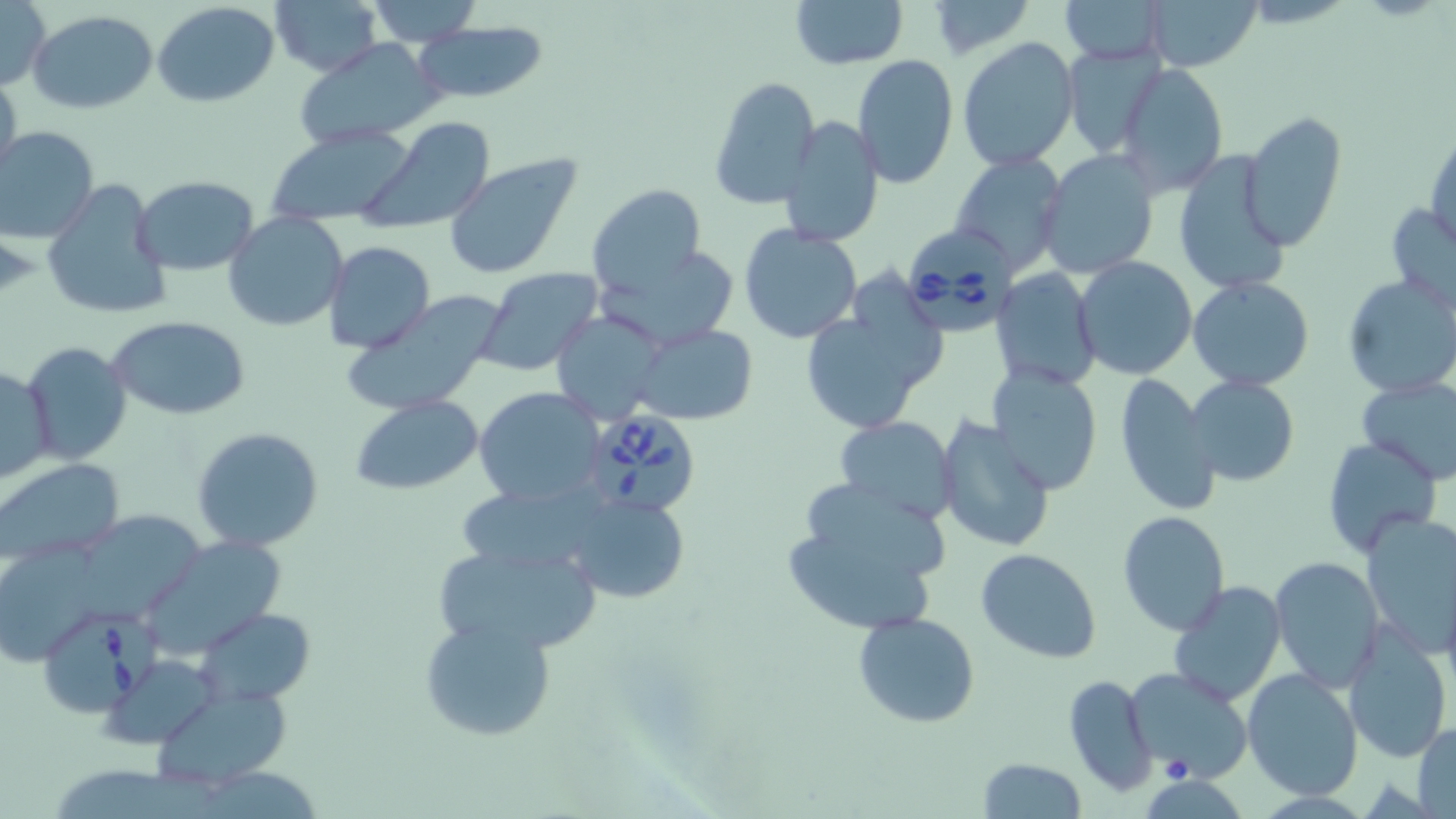

Summary:
  - Coordinate format: approximate bounding boxes as (x1, y1, x2, y2) in pixels
  - Babesia divergens-infected red blood cell locations: (901, 224, 1021, 337), (579, 403, 699, 519), (39, 607, 154, 718)
  - Uninfected red blood cell locations: (0, 0, 50, 91), (267, 0, 384, 78), (364, 0, 480, 47), (789, 0, 908, 71), (928, 0, 1033, 59), (1143, 0, 1264, 71), (1061, 1, 1168, 65), (152, 2, 280, 108), (28, 10, 157, 115), (414, 21, 550, 103), (956, 36, 1081, 172), (295, 38, 447, 150), (1062, 41, 1165, 160), (850, 55, 959, 190), (1115, 62, 1229, 195), (0, 70, 22, 191), (709, 75, 818, 211), (1240, 112, 1349, 251), (359, 116, 496, 232), (778, 116, 885, 247), (0, 125, 100, 243), (264, 127, 415, 225), (1426, 127, 1456, 254), (1037, 149, 1161, 279), (442, 152, 584, 280), (949, 153, 1069, 275), (1170, 153, 1291, 296), (132, 176, 260, 274), (40, 177, 170, 323), (587, 182, 706, 297), (1385, 201, 1456, 313), (224, 212, 348, 332), (739, 223, 863, 344), (321, 241, 435, 354), (599, 255, 741, 344), (1074, 256, 1198, 379), (477, 268, 603, 375), (991, 270, 1102, 390), (1342, 274, 1456, 398), (1188, 276, 1315, 390), (800, 284, 948, 438), (339, 292, 504, 415), (549, 310, 667, 421), (106, 316, 251, 420), (634, 324, 757, 425), (21, 341, 134, 465), (1, 363, 55, 487), (986, 366, 1103, 497), (1112, 373, 1218, 515), (1187, 376, 1298, 488), (1356, 378, 1456, 484), (472, 385, 606, 508), (351, 395, 485, 495), (935, 414, 1056, 555), (833, 416, 957, 523), (191, 426, 326, 553), (1320, 436, 1442, 556), (0, 457, 126, 567), (779, 479, 954, 637), (457, 488, 602, 574), (569, 492, 690, 602), (1117, 511, 1229, 637), (1361, 512, 1456, 658), (81, 513, 204, 618), (150, 535, 294, 653), (432, 542, 604, 657), (0, 545, 105, 660), (977, 548, 1100, 664), (1270, 557, 1384, 692), (1168, 580, 1287, 705), (196, 607, 315, 706), (852, 612, 981, 729), (419, 616, 557, 742), (1343, 629, 1454, 764), (106, 662, 222, 745), (1125, 668, 1255, 781), (1243, 669, 1364, 798), (1063, 672, 1157, 797), (153, 688, 295, 786), (1412, 719, 1455, 816), (978, 758, 1087, 818)
  - Slide-level diagnosis: Babesia divergens
  - Preparation: thin blood smear
  - Image size: 1456×819 pixels
  - Magnification: 1000x
  - Modality: light microscopy
  - Stain: May-Grünwald-Giemsa
  - Field of view: single